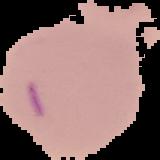
Image is 160×160 pixels. Malaria status: uninfected. Segmented cell region on a black background. From a thin blood smear.